Give the position of each P. falciparum parasite with its life-cycle stage, each leukocyte, and any debris.
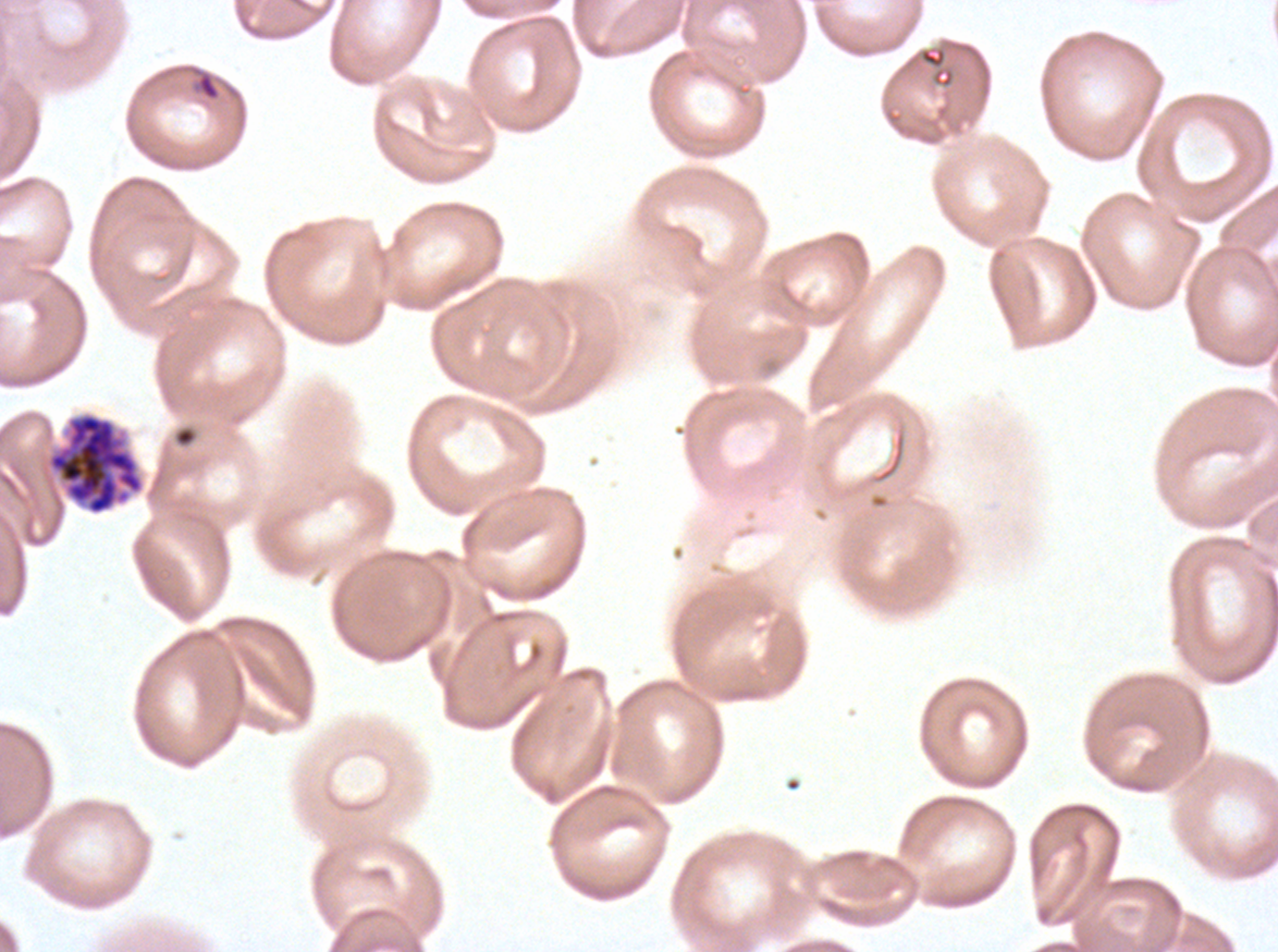

Approximate bounding boxes as [x1, y1, x2, y2] in pixels.
Rings: [190, 66, 222, 102].
Segmenters: [45, 411, 145, 516].
No late-ring/early-trophozoite forms, mid trophozoites, late trophozoites, early schizonts, late schizonts, gametocytes, leukocytes, or debris observed.

Summary:
  - Image size: 1278×952 pixels
  - Stain: Giemsa
  - Field of view: sub-image separated from a larger composite
  - Life-cycle stages observed: ring, segmenter
  - Specimen: P. falciparum from a patient in The Gambia, cultured ex vivo for 24 to 48 hours
  - Preparation: thin blood smear